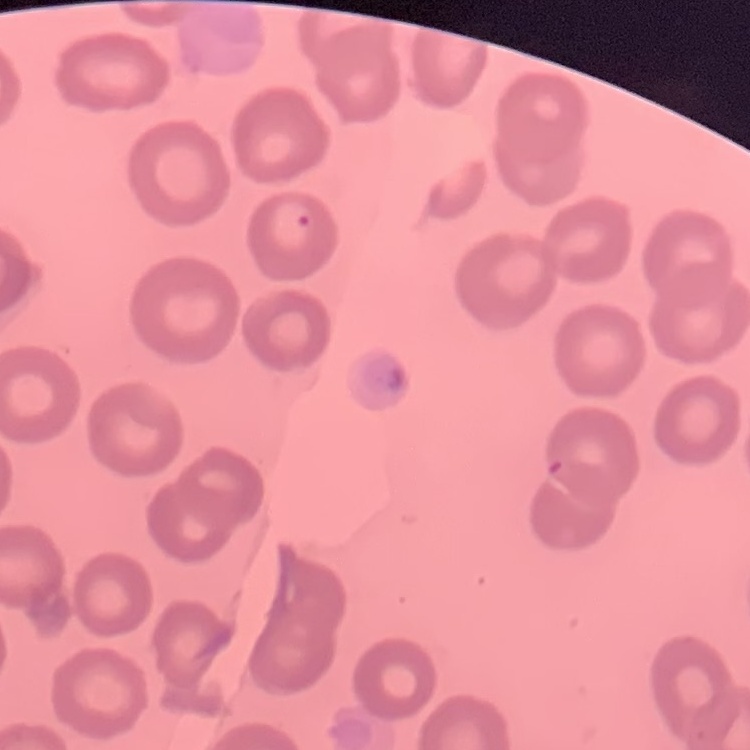 The erythrocytes exhibit no rouleaux formation. Field's or Giemsa stain. Thin blood smear. One tile cut from a larger photomicrograph.